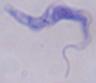

modality: photomicrograph
identification: trypanosome
magnification: 1000x